Assess this cell for malaria.
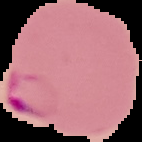
It is parasitized.

Cell region segmented out of the field of view; the surrounding area is masked to black. Image is 142×142 pixels. From a thin blood film.